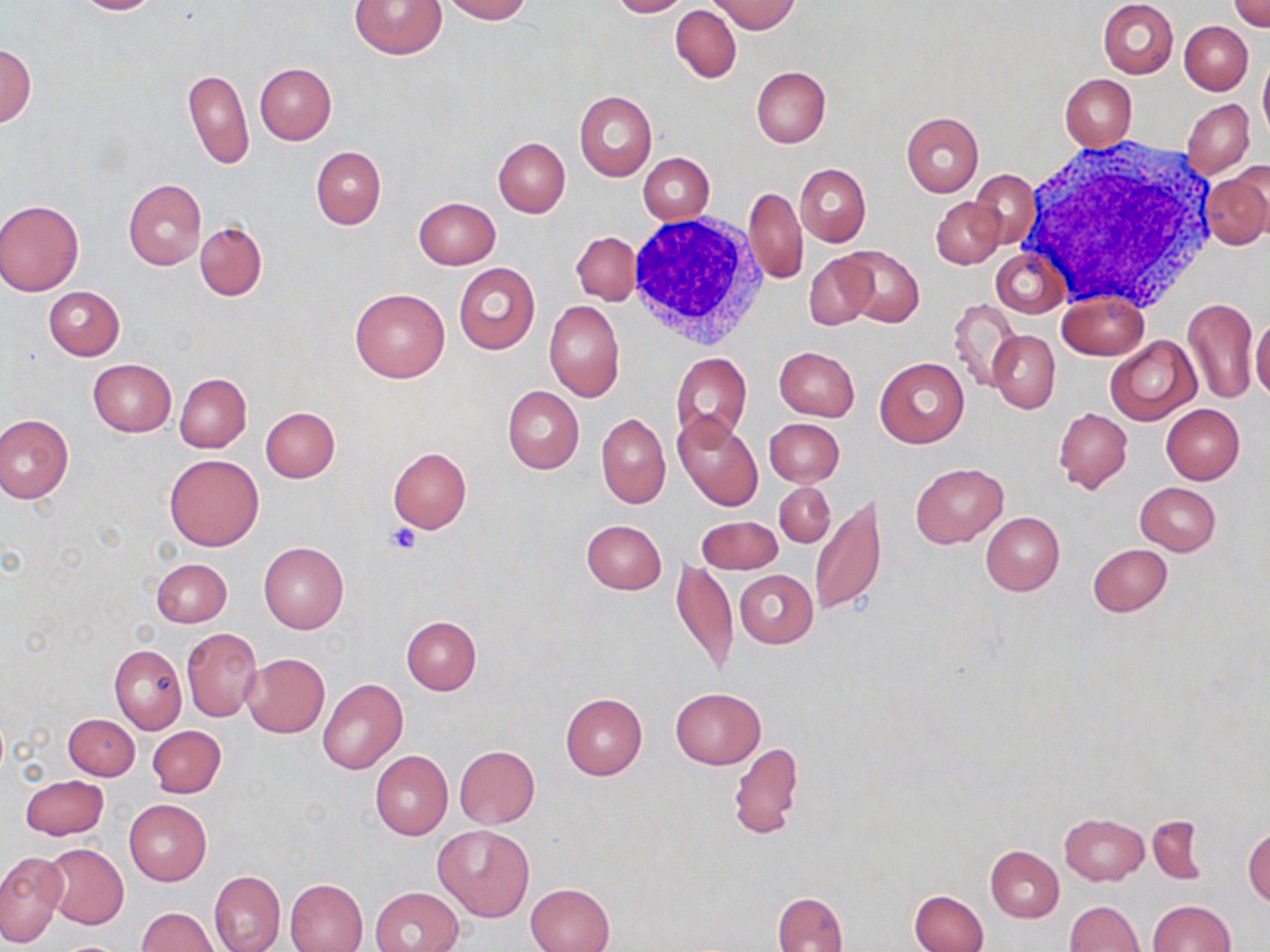
Approximate bounding boxes as [x1, y1, x2, y2] in pixels. Uninfected red blood cell locations: [72, 0, 163, 15], [350, 0, 447, 59], [440, 0, 530, 22], [607, 0, 688, 17], [1098, 0, 1178, 78], [710, 1, 800, 33], [1230, 2, 1270, 33], [671, 6, 741, 81], [1180, 21, 1253, 94], [1, 44, 36, 127], [1258, 52, 1270, 142], [255, 62, 337, 144], [182, 65, 254, 169], [751, 67, 830, 148], [1060, 74, 1137, 150], [574, 90, 655, 181], [1182, 98, 1254, 176], [900, 112, 983, 196], [494, 138, 570, 218], [311, 147, 385, 229], [639, 152, 714, 223], [796, 163, 871, 246], [1202, 168, 1270, 251], [969, 169, 1038, 249], [124, 179, 206, 269], [744, 187, 807, 283], [413, 198, 500, 269], [932, 198, 1005, 269], [0, 200, 84, 295], [195, 221, 267, 301], [571, 231, 641, 306], [842, 246, 923, 325], [992, 249, 1066, 317], [803, 250, 880, 330], [454, 263, 540, 355], [44, 286, 125, 360], [350, 288, 449, 384], [1057, 293, 1149, 360], [1182, 297, 1258, 405], [949, 299, 1020, 391], [544, 300, 624, 402], [1250, 316, 1270, 403], [988, 331, 1059, 413], [1104, 335, 1200, 426], [773, 347, 860, 420], [671, 352, 752, 443], [874, 357, 969, 447], [87, 360, 175, 437], [175, 373, 251, 452], [502, 386, 584, 474], [1161, 403, 1244, 484], [260, 406, 339, 482], [1053, 408, 1131, 493], [0, 413, 73, 504], [597, 413, 670, 509], [672, 413, 763, 511], [764, 419, 844, 487], [388, 447, 472, 533], [164, 454, 264, 551], [912, 463, 1007, 547], [775, 482, 835, 547], [1136, 483, 1221, 555], [810, 493, 887, 616], [981, 512, 1064, 596], [696, 517, 782, 573], [580, 520, 666, 595], [259, 542, 348, 633], [1088, 544, 1172, 617], [151, 558, 232, 627], [670, 559, 738, 675], [734, 570, 817, 647], [401, 617, 480, 694], [182, 627, 261, 722], [110, 645, 186, 734], [241, 653, 329, 738], [318, 679, 407, 773], [670, 687, 765, 768], [561, 693, 647, 779], [63, 714, 138, 780], [148, 726, 225, 797], [729, 741, 803, 842], [455, 745, 539, 828], [371, 751, 453, 839], [21, 775, 107, 839], [123, 800, 211, 886], [1059, 813, 1149, 885], [1148, 815, 1205, 884], [433, 825, 534, 921], [1243, 825, 1270, 906], [42, 844, 128, 928], [985, 845, 1064, 921], [0, 851, 68, 947], [210, 870, 285, 952], [285, 878, 368, 952], [525, 883, 613, 951], [371, 887, 462, 952], [909, 890, 989, 952], [773, 891, 847, 952], [1145, 900, 1235, 952], [1066, 901, 1143, 952], [137, 907, 219, 952]. Platelet locations: [387, 523, 420, 555]. White blood cell locations: [1018, 137, 1221, 313], [623, 213, 770, 350]. Slide-level diagnosis: negative for blood parasites. Light microscopy. May-Grünwald-Giemsa stain. Captured at 1000x magnification. Single field of view. Thin blood film. Image is 1270×952 pixels.